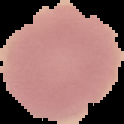

The area outside the segmented cell region is set to black. Malaria status: uninfected. From a thin blood smear. Image is 124×124 pixels.